Report the malaria status of this cell.
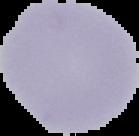
It is uninfected.

Image is 139×136 pixels. The area outside the segmented cell region is set to black. From a thin blood film.